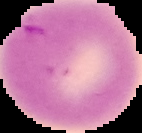
{
  "preparation": "thin blood film",
  "image_type": "segmented cell region on a black background",
  "image_size": "142×133 pixels",
  "malaria_status": "uninfected"
}